Report the malaria status.
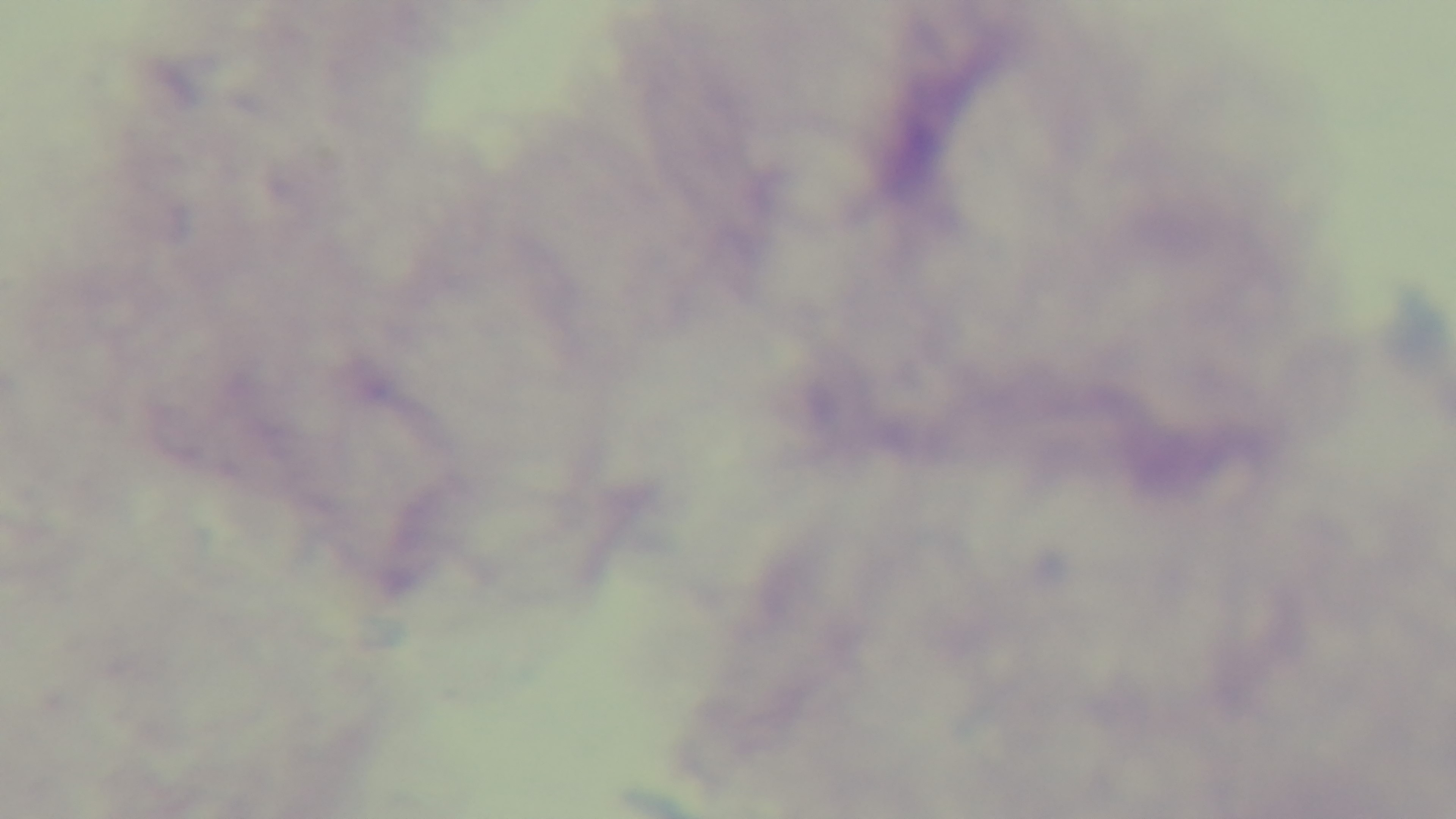
It is uninfected.

Summary:
  - Field of view: single
  - Modality: light microscopy
  - Stain: Giemsa
  - Preparation: thick smear
  - Objective: 100x oil immersion
  - Capture: mounted 4K digital camera